Locate every leukocyte (white blood cell).
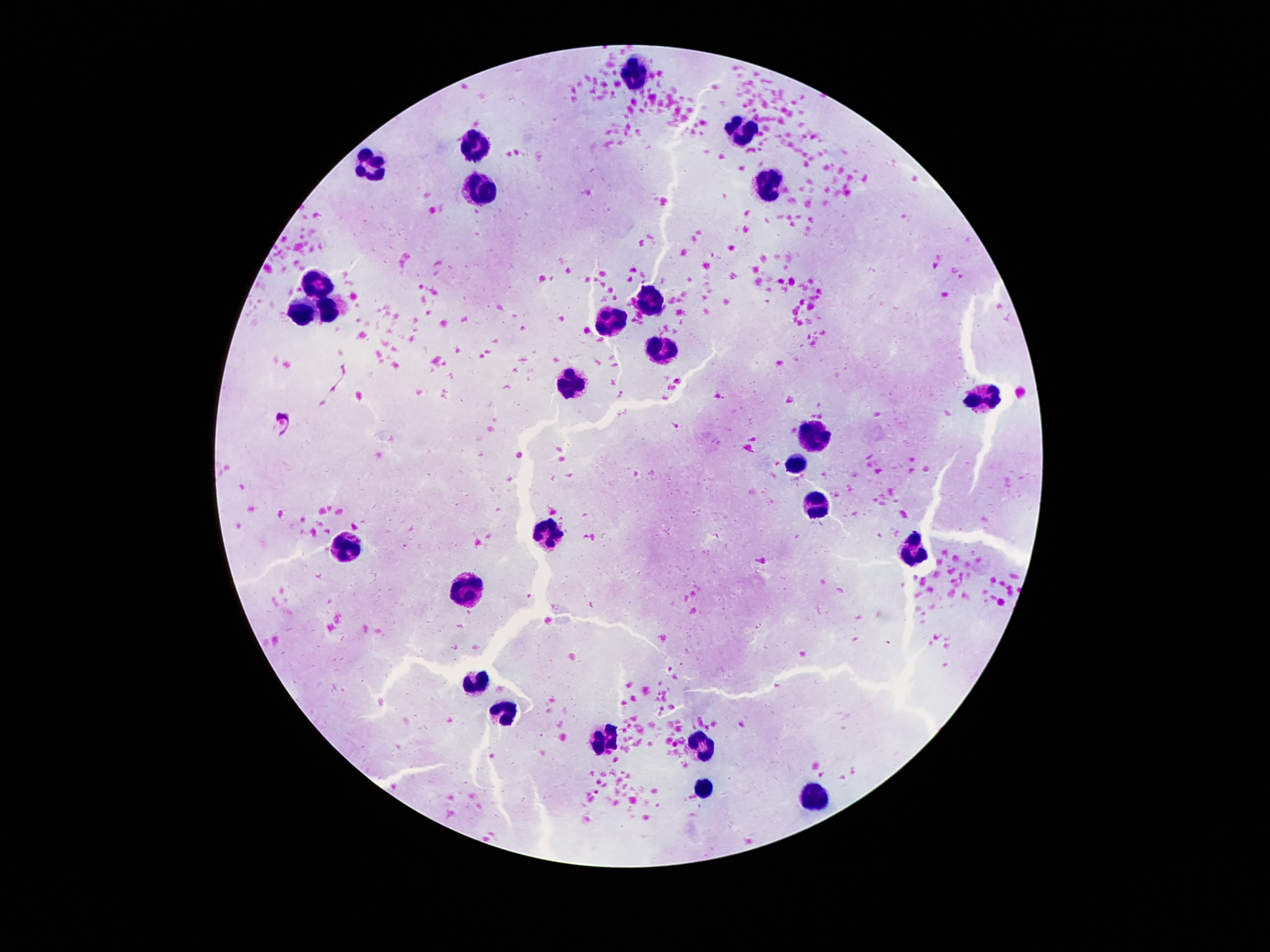

Approximate centers as (x, y) in pixels.
Leukocytes: (635, 78), (742, 128), (473, 139), (368, 166), (765, 182), (480, 189), (318, 284), (656, 300), (328, 309), (305, 313), (608, 321), (662, 348), (568, 387), (979, 397), (814, 433), (795, 465), (814, 499), (549, 530), (345, 549), (912, 551), (469, 590), (475, 683), (503, 714), (605, 740), (700, 746), (706, 790), (813, 799).

magnification = 100x
patient malaria status = negative
image size = 1270×952 pixels
capture = smartphone camera through the microscope eyepiece
stain = Giemsa
preparation = thick blood film
field of view = single